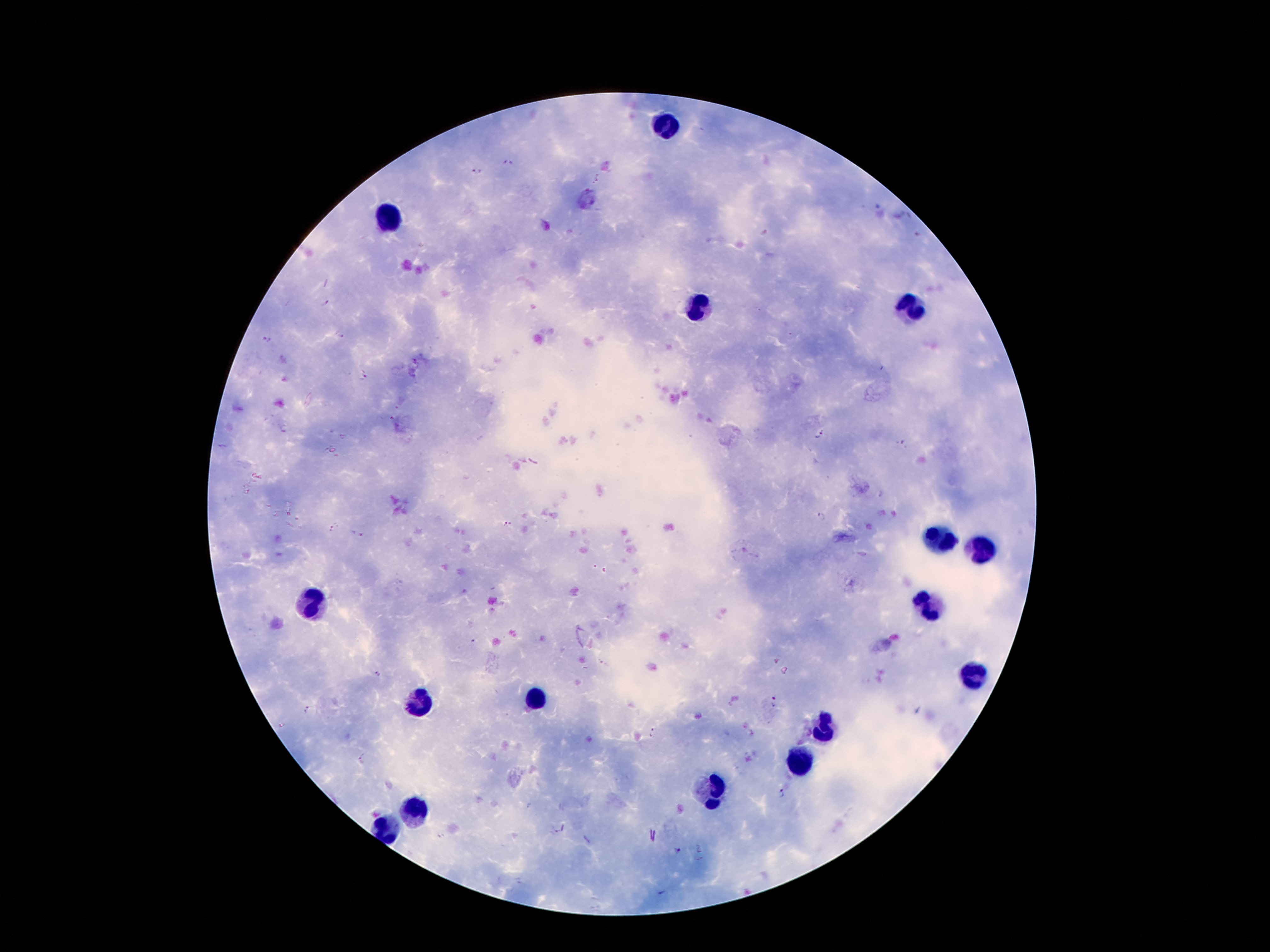
Approximate object centers, in pixels from the top-left corner. Malaria parasite locations: (x=508, y=162), (x=478, y=171), (x=599, y=178), (x=764, y=231), (x=917, y=234), (x=325, y=303), (x=339, y=336), (x=267, y=338), (x=365, y=376), (x=821, y=434), (x=902, y=443), (x=822, y=515), (x=507, y=524), (x=335, y=529), (x=357, y=533), (x=604, y=664), (x=378, y=674), (x=774, y=701), (x=309, y=709), (x=654, y=733), (x=363, y=759), (x=780, y=793), (x=554, y=831), (x=440, y=836), (x=676, y=851), (x=662, y=892). Leukocyte locations: (x=662, y=127), (x=387, y=218), (x=699, y=310), (x=914, y=315), (x=936, y=542), (x=980, y=552), (x=311, y=604), (x=928, y=609), (x=975, y=675), (x=419, y=702), (x=535, y=702), (x=822, y=727), (x=795, y=762), (x=711, y=789), (x=412, y=814), (x=387, y=831). Single field of view. Thick blood smear. Photographed through the microscope eyepiece with a smartphone camera. Image is 1270×952 pixels. Patient malaria status: infected with Plasmodium falciparum. Giemsa stain. 100x magnification.